Locate every blood parasite and identify its species.
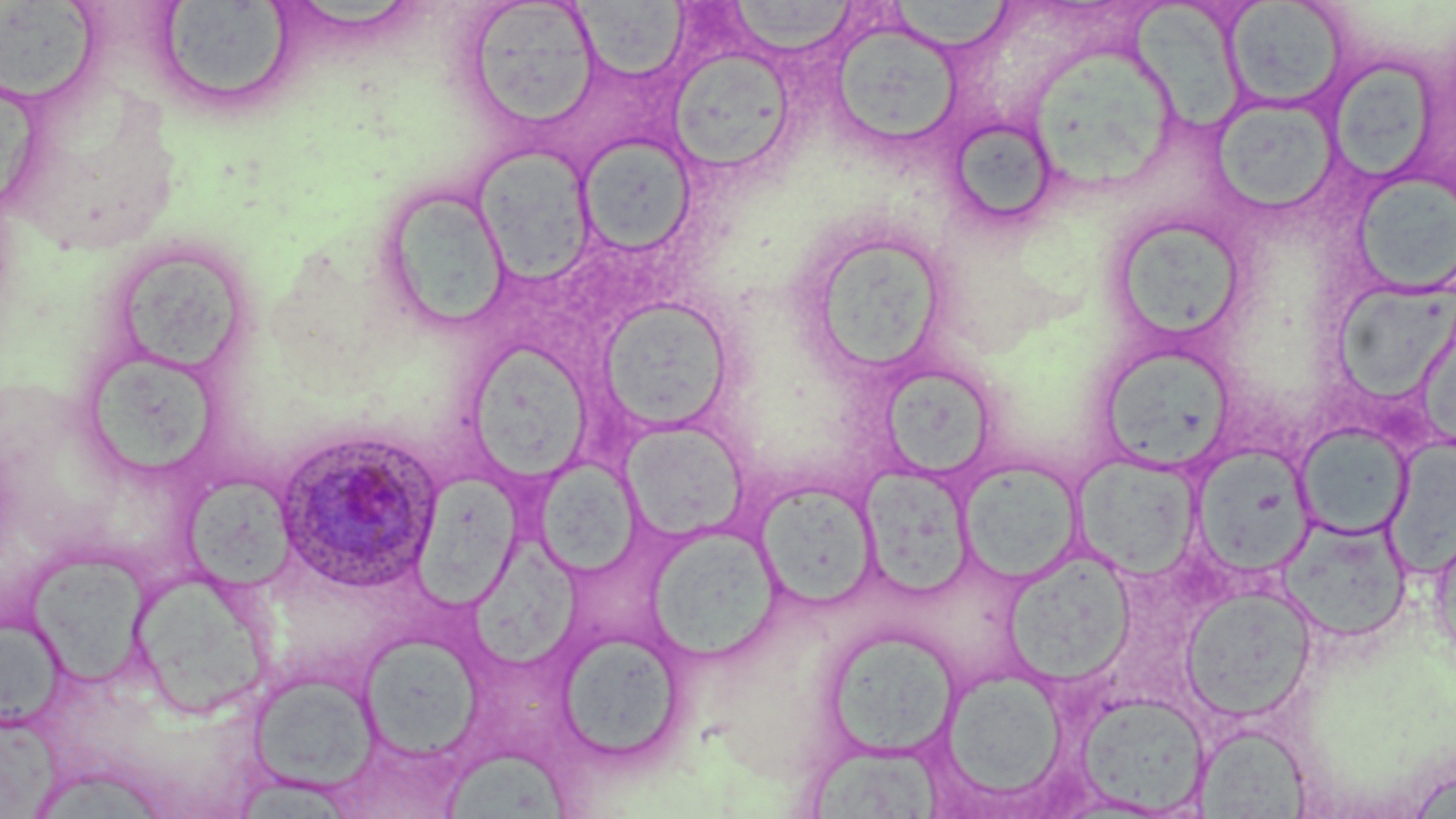

Approximate bounding boxes as named x1/y1/x2/y2 corners in pixels.
Plasmodium ovale-infected red blood cells: (x1=273, y1=427, x2=443, y2=593).
No Plasmodium falciparum, Plasmodium malariae, Plasmodium vivax, Babesia divergens, or Trypanosoma brucei observed.

Uninfected red blood cell locations: (x1=4, y1=0, x2=105, y2=108), (x1=462, y1=0, x2=604, y2=132), (x1=1130, y1=0, x2=1245, y2=135), (x1=156, y1=1, x2=296, y2=112), (x1=727, y1=1, x2=859, y2=55), (x1=888, y1=1, x2=1015, y2=51), (x1=1224, y1=1, x2=1348, y2=110), (x1=574, y1=2, x2=690, y2=79), (x1=830, y1=17, x2=965, y2=149), (x1=1026, y1=41, x2=1180, y2=191), (x1=670, y1=46, x2=796, y2=173), (x1=1330, y1=59, x2=1440, y2=182), (x1=1211, y1=97, x2=1341, y2=217), (x1=945, y1=116, x2=1062, y2=231), (x1=578, y1=135, x2=698, y2=255), (x1=471, y1=147, x2=598, y2=285), (x1=1351, y1=172, x2=1456, y2=295), (x1=376, y1=186, x2=512, y2=331), (x1=1107, y1=214, x2=1248, y2=347), (x1=820, y1=234, x2=944, y2=373), (x1=119, y1=254, x2=240, y2=372), (x1=1341, y1=279, x2=1456, y2=401), (x1=597, y1=298, x2=735, y2=433), (x1=469, y1=336, x2=590, y2=486), (x1=1103, y1=349, x2=1237, y2=475), (x1=84, y1=358, x2=225, y2=475), (x1=871, y1=368, x2=996, y2=481), (x1=621, y1=421, x2=750, y2=541), (x1=1295, y1=422, x2=1413, y2=539), (x1=1191, y1=443, x2=1316, y2=577), (x1=1073, y1=453, x2=1201, y2=578), (x1=535, y1=455, x2=638, y2=576), (x1=959, y1=459, x2=1083, y2=583), (x1=860, y1=466, x2=974, y2=597), (x1=413, y1=469, x2=530, y2=623), (x1=183, y1=473, x2=297, y2=589), (x1=755, y1=480, x2=880, y2=609), (x1=1277, y1=514, x2=1413, y2=642), (x1=647, y1=525, x2=782, y2=663), (x1=1429, y1=526, x2=1455, y2=675), (x1=468, y1=533, x2=591, y2=675), (x1=25, y1=549, x2=154, y2=687), (x1=1002, y1=549, x2=1137, y2=684), (x1=130, y1=564, x2=274, y2=718), (x1=1181, y1=586, x2=1316, y2=721), (x1=0, y1=619, x2=72, y2=738), (x1=823, y1=627, x2=960, y2=759), (x1=555, y1=631, x2=686, y2=764), (x1=357, y1=632, x2=484, y2=760), (x1=933, y1=667, x2=1071, y2=809), (x1=246, y1=670, x2=382, y2=795), (x1=1074, y1=691, x2=1211, y2=815), (x1=0, y1=714, x2=68, y2=819), (x1=1195, y1=723, x2=1312, y2=817), (x1=444, y1=747, x2=571, y2=819), (x1=811, y1=749, x2=944, y2=819), (x1=43, y1=773, x2=172, y2=819). Slide-level diagnosis: Plasmodium ovale. One field of a larger specimen. Image is 1456×819 pixels. May-Grünwald-Giemsa-stained preparation. Thin blood film. 1000x magnification. Optical microscopy.